Report the malaria status of this cell.
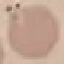

It is uninfected.

image type = automatically extracted cell patch, resized to 64 × 64 pixels
preparation = thin blood smear
stain = Giemsa
capture = smartphone camera at the microscope eyepiece